Report the malaria status of this cell.
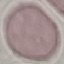
Uninfected.

{
  "stain": "Giemsa",
  "capture": "smartphone camera at the microscope eyepiece",
  "image_type": "automatically extracted cell patch, resized to 64 × 64 pixels",
  "preparation": "thin smear"
}